Identify the blood parasite species.
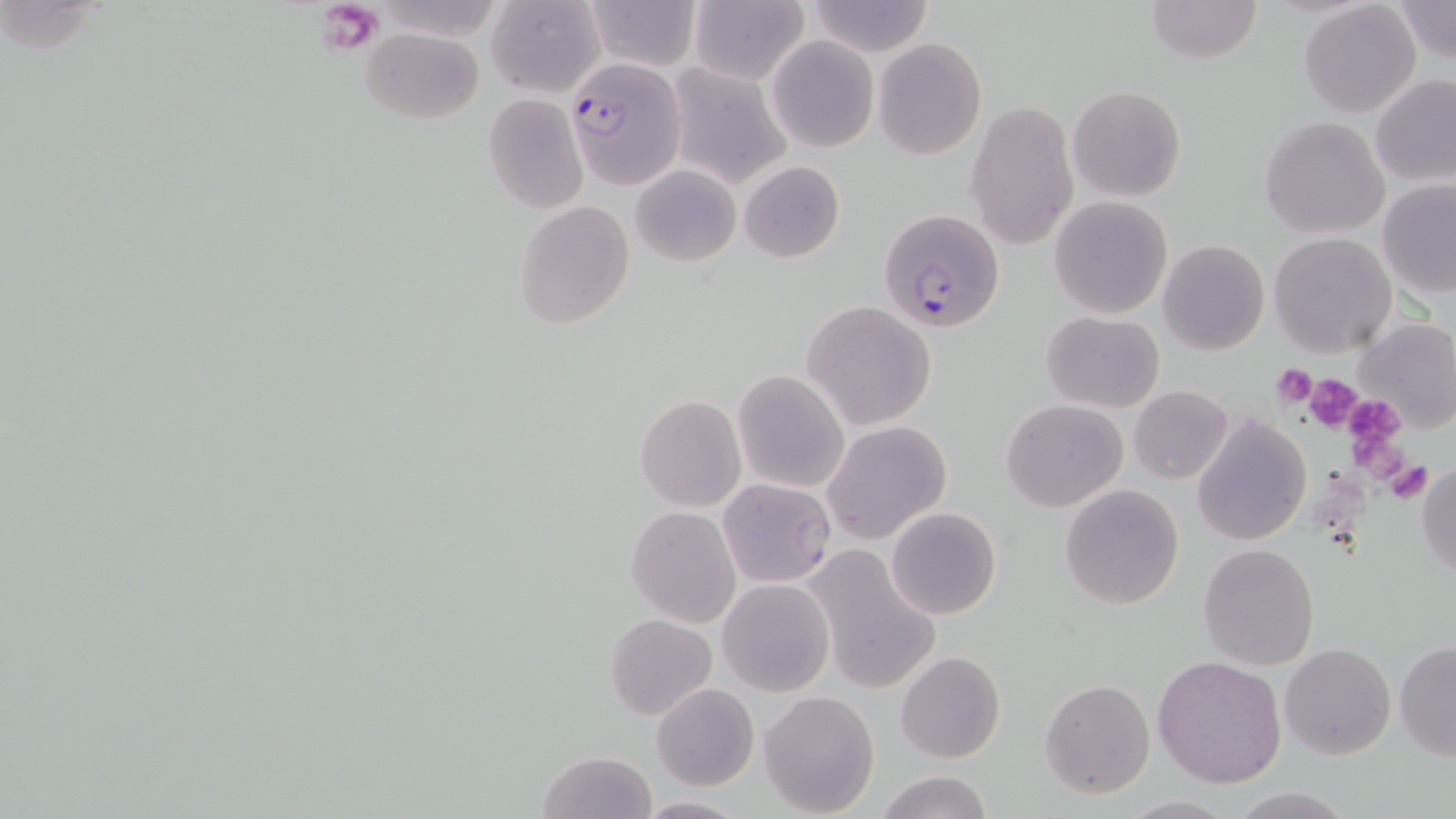

Plasmodium falciparum.

Summary:
  - Coordinate format: approximate bounding boxes as named x1/y1/x2/y2 corners in pixels
  - Platelet locations: (x1=319, y1=1, x2=384, y2=50), (x1=1272, y1=364, x2=1318, y2=408), (x1=1303, y1=373, x2=1364, y2=433), (x1=1353, y1=403, x2=1404, y2=454), (x1=1354, y1=433, x2=1402, y2=480), (x1=1387, y1=459, x2=1431, y2=505)
  - Uninfected red blood cell locations: (x1=585, y1=0, x2=701, y2=72), (x1=1146, y1=0, x2=1262, y2=65), (x1=1392, y1=0, x2=1455, y2=66), (x1=806, y1=1, x2=933, y2=55), (x1=1298, y1=1, x2=1421, y2=118), (x1=485, y1=2, x2=605, y2=95), (x1=688, y1=2, x2=809, y2=84), (x1=363, y1=27, x2=482, y2=123), (x1=766, y1=35, x2=878, y2=152), (x1=873, y1=38, x2=986, y2=160), (x1=666, y1=63, x2=792, y2=187), (x1=1371, y1=74, x2=1456, y2=188), (x1=1068, y1=85, x2=1185, y2=202), (x1=483, y1=94, x2=588, y2=213), (x1=964, y1=99, x2=1080, y2=250), (x1=1260, y1=116, x2=1389, y2=238), (x1=739, y1=160, x2=845, y2=263), (x1=631, y1=164, x2=741, y2=267), (x1=1378, y1=180, x2=1456, y2=297), (x1=1049, y1=196, x2=1173, y2=318), (x1=515, y1=200, x2=634, y2=330), (x1=1270, y1=232, x2=1396, y2=357), (x1=1157, y1=239, x2=1269, y2=355), (x1=801, y1=302, x2=937, y2=429), (x1=1043, y1=311, x2=1164, y2=411), (x1=1357, y1=318, x2=1456, y2=433), (x1=733, y1=372, x2=849, y2=492), (x1=1129, y1=385, x2=1235, y2=484), (x1=634, y1=395, x2=746, y2=512), (x1=1002, y1=400, x2=1127, y2=511), (x1=1192, y1=415, x2=1310, y2=546), (x1=822, y1=420, x2=951, y2=544), (x1=1416, y1=463, x2=1456, y2=578), (x1=717, y1=478, x2=836, y2=587), (x1=1059, y1=485, x2=1184, y2=607), (x1=886, y1=506, x2=1000, y2=620), (x1=626, y1=507, x2=741, y2=626), (x1=1198, y1=544, x2=1320, y2=670), (x1=805, y1=546, x2=941, y2=694), (x1=719, y1=580, x2=832, y2=695), (x1=605, y1=614, x2=717, y2=721), (x1=1394, y1=642, x2=1456, y2=760), (x1=1280, y1=644, x2=1396, y2=761), (x1=896, y1=650, x2=1005, y2=764), (x1=1154, y1=655, x2=1287, y2=789), (x1=1040, y1=679, x2=1155, y2=799), (x1=651, y1=684, x2=759, y2=790), (x1=759, y1=692, x2=879, y2=817), (x1=536, y1=750, x2=657, y2=819), (x1=876, y1=772, x2=993, y2=819), (x1=1223, y1=788, x2=1360, y2=818), (x1=632, y1=796, x2=750, y2=816)
  - Plasmodium falciparum-infected red blood cell locations: (x1=568, y1=59, x2=687, y2=188), (x1=880, y1=209, x2=1003, y2=334)
  - Field of view: one of a larger specimen
  - Magnification: 1000x
  - Modality: light microscopy
  - Stain: May-Grünwald-Giemsa
  - Image size: 1456×819 pixels
  - Preparation: thin blood smear